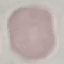

Result: no malaria parasites seen. Cell patch, automatically extracted from a larger field of view and resized to 64 × 64 pixels. Thin blood film. Giemsa-stained preparation. Photographed with a smartphone camera at the microscope eyepiece.